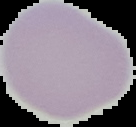 The area outside the segmented cell region is set to black. Image is 136×127 pixels. From a thin blood film. Result: negative for malaria parasites.